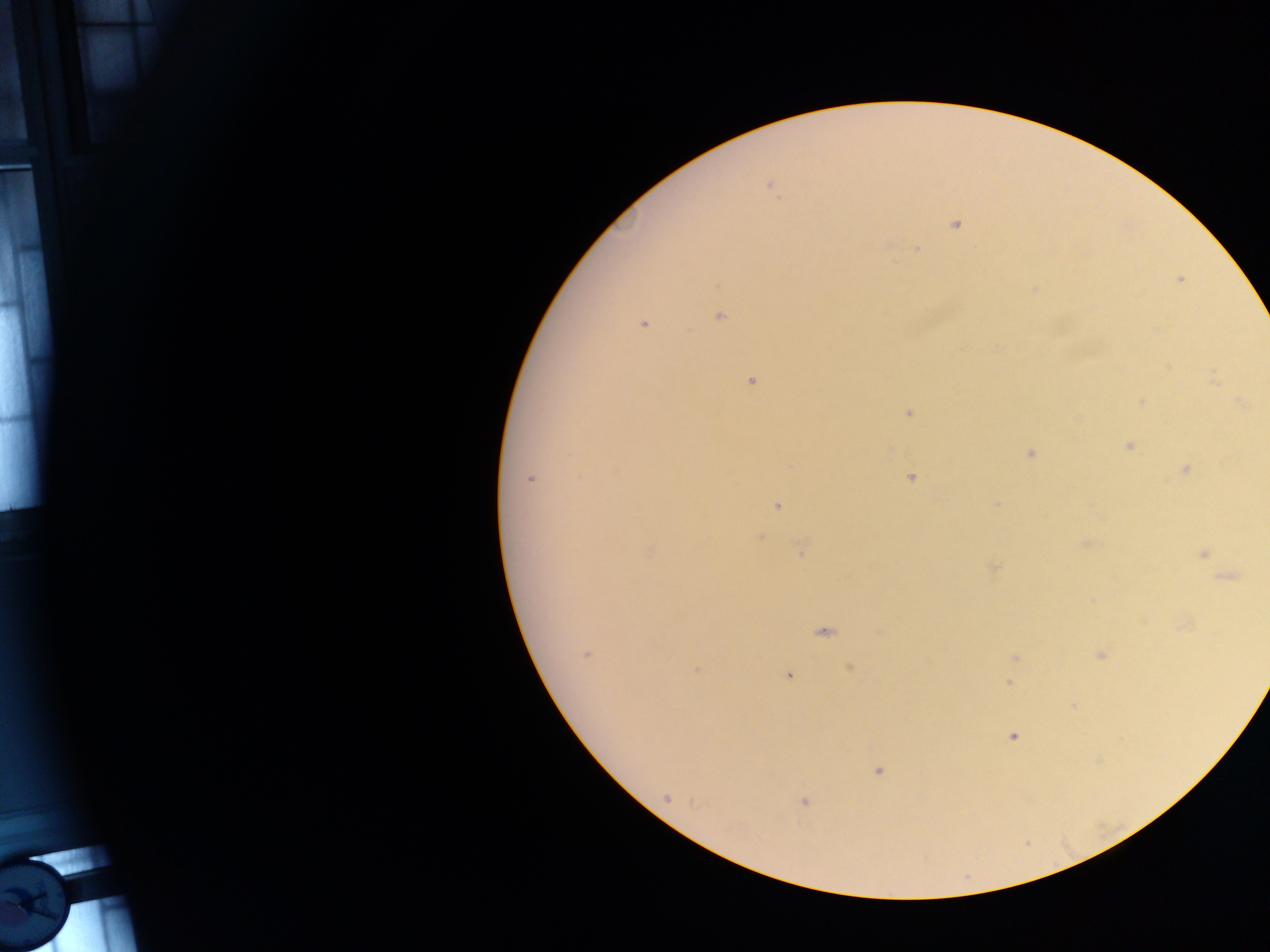
Approximate centers as (x, y) in pixels. Malaria parasite locations: (771, 186), (955, 224), (916, 248), (1179, 279), (1034, 288), (719, 317), (644, 325), (1212, 380), (751, 382), (1141, 401), (1241, 403), (907, 413), (1129, 446), (1031, 453), (1185, 468), (910, 477), (530, 478), (996, 505), (777, 506), (802, 549), (650, 551), (1202, 553), (995, 568), (1229, 577), (823, 632), (586, 654), (1101, 655), (1015, 657), (851, 668), (696, 670), (789, 675), (1010, 683), (1013, 737), (878, 771), (667, 798), (803, 802). Photographed through a microscope with a mobile-phone camera. Image is 1270×952 pixels. Single field of view. Collected in Ghana. Thick blood film.